Identify the parasite.
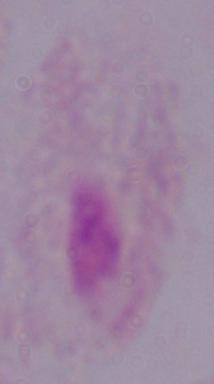

This is a trichomonad.

Summary:
  - Magnification: 1000x
  - Modality: photomicrograph